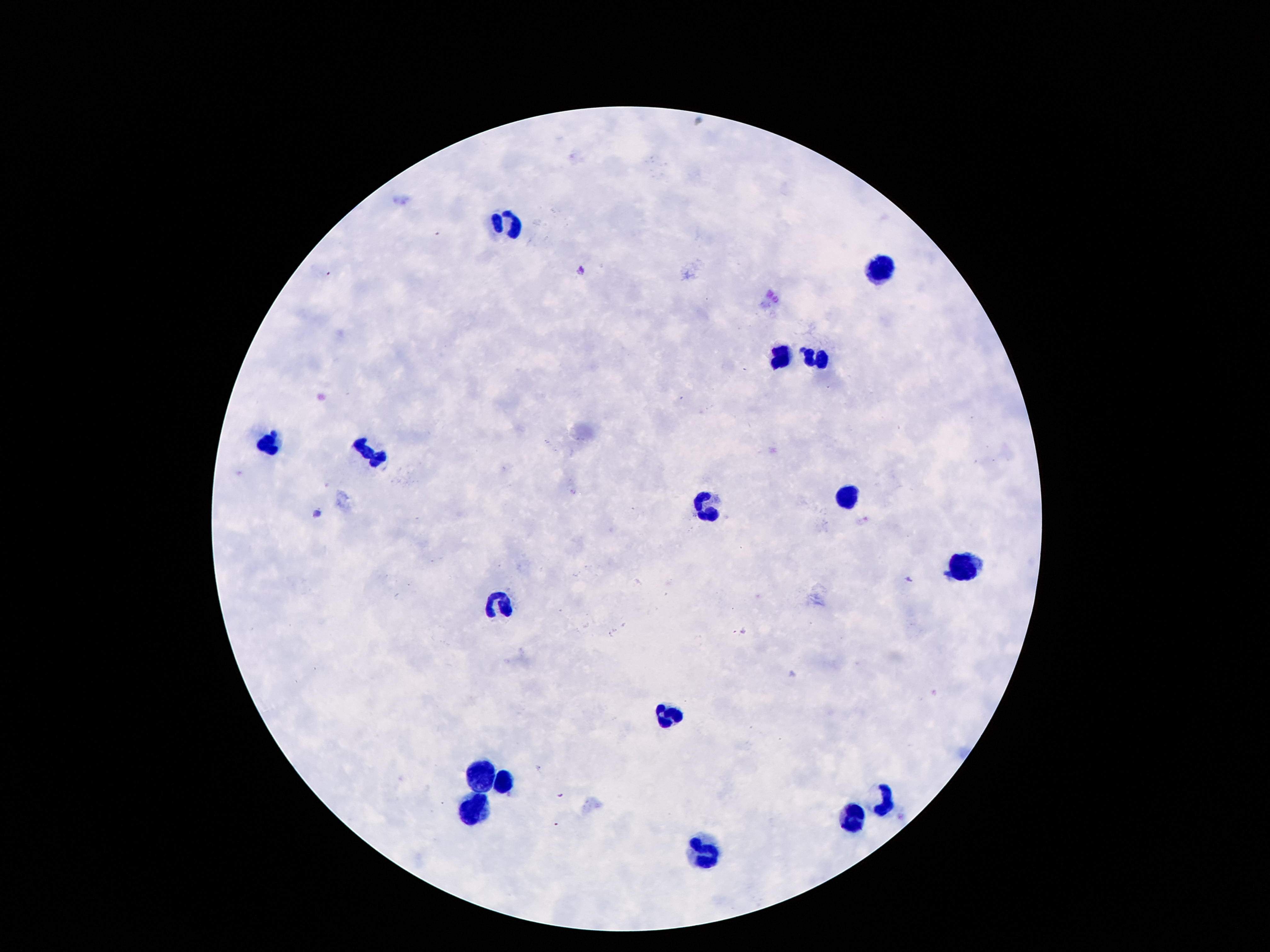
image size = 1270×952 pixels
stain = Giemsa
patient malaria status = uninfected
preparation = thick blood film
leukocyte locations = approximate centers as [x, y] in pixels: [506, 218], [878, 264], [779, 358], [818, 361], [263, 442], [372, 452], [846, 496], [706, 508], [960, 569], [499, 602], [668, 714], [480, 776], [504, 783], [885, 800], [471, 809], [848, 822], [702, 852]
field of view = one from this slide
magnification = 100x
capture = smartphone camera through the microscope eyepiece